Identify the blood parasite species.
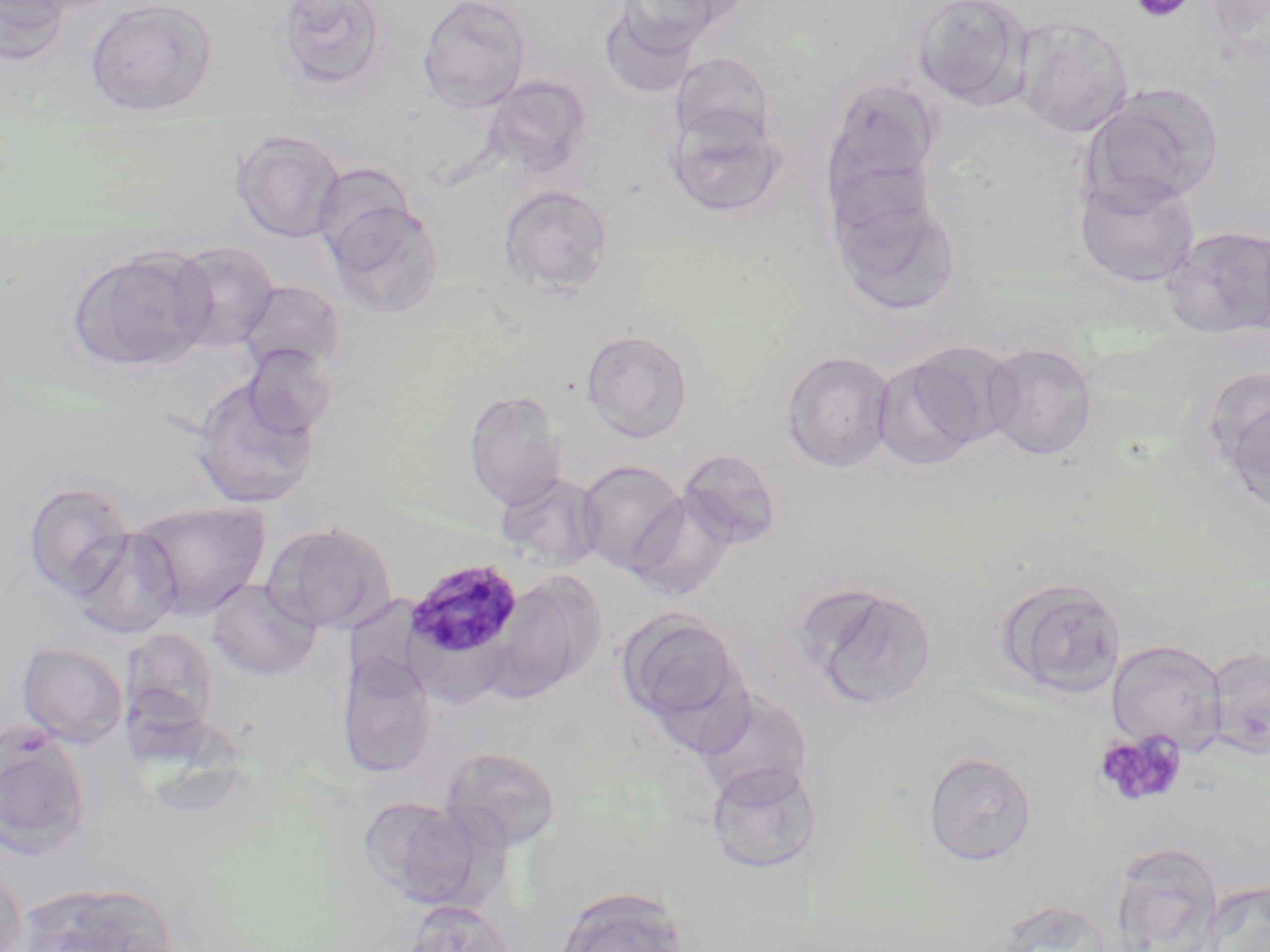
Plasmodium malariae.

image size = 1270×952 pixels
Plasmodium malariae-infected red blood cell locations = approximate bounding boxes as [x1, y1, x2, y2] in pixels: [402, 558, 526, 665]
uninfected red blood cell locations = approximate bounding boxes as [x1, y1, x2, y2] in pixels: [0, 0, 72, 64], [6, 0, 124, 16], [86, 0, 218, 116], [418, 0, 531, 112], [914, 0, 1031, 108], [277, 1, 388, 90], [608, 2, 740, 57], [1013, 16, 1134, 137], [481, 76, 593, 179], [823, 79, 940, 202], [1085, 82, 1225, 210], [664, 103, 786, 218], [232, 129, 345, 243], [312, 163, 417, 263], [1074, 173, 1200, 287], [498, 184, 613, 295], [830, 188, 962, 316], [324, 198, 444, 318], [1162, 226, 1270, 339], [168, 241, 280, 351], [68, 246, 215, 371], [238, 279, 345, 377], [580, 329, 694, 442], [981, 342, 1098, 462], [241, 343, 336, 437], [781, 349, 896, 473], [873, 351, 991, 471], [1208, 372, 1270, 513], [192, 378, 321, 510], [463, 389, 567, 510], [678, 449, 781, 547], [576, 460, 688, 576], [494, 471, 604, 570], [22, 481, 136, 601], [626, 491, 736, 601], [128, 500, 271, 619], [264, 521, 397, 635], [70, 527, 183, 640], [490, 573, 601, 700], [996, 577, 1127, 699], [207, 580, 321, 680], [798, 582, 939, 711], [618, 609, 747, 731], [1107, 639, 1226, 753], [17, 642, 129, 748], [1205, 647, 1270, 760], [336, 650, 437, 778], [693, 688, 814, 805], [0, 728, 92, 858], [440, 745, 563, 852], [923, 751, 1037, 866], [705, 760, 822, 874], [359, 796, 482, 908], [1106, 843, 1224, 952], [0, 870, 27, 952], [1199, 880, 1270, 951], [17, 881, 179, 952], [553, 885, 691, 952], [402, 900, 515, 952]
modality = light microscopy
preparation = thin blood film
magnification = 1000x
field of view = single
stain = May-Grünwald-Giemsa
platelet locations = approximate bounding boxes as [x1, y1, x2, y2] in pixels: [1131, 0, 1196, 23], [1095, 730, 1186, 809]